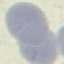

{
  "result": "no malaria parasites seen",
  "capture": "smartphone through the microscope eyepiece",
  "image_type": "cell patch, automatically extracted from a larger field of view and resized to 64 × 64 pixels",
  "stain": "Giemsa",
  "preparation": "thin blood smear"
}